Report the malaria status of this cell.
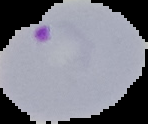
It is parasitized.

{
  "image_size": "148×124 pixels",
  "image_type": "segmented cell region with the area outside set to black",
  "preparation": "thin blood film"
}